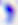

Summary:
  - Identification: Toxoplasma gondii
  - Magnification: 400x
  - Modality: micrograph